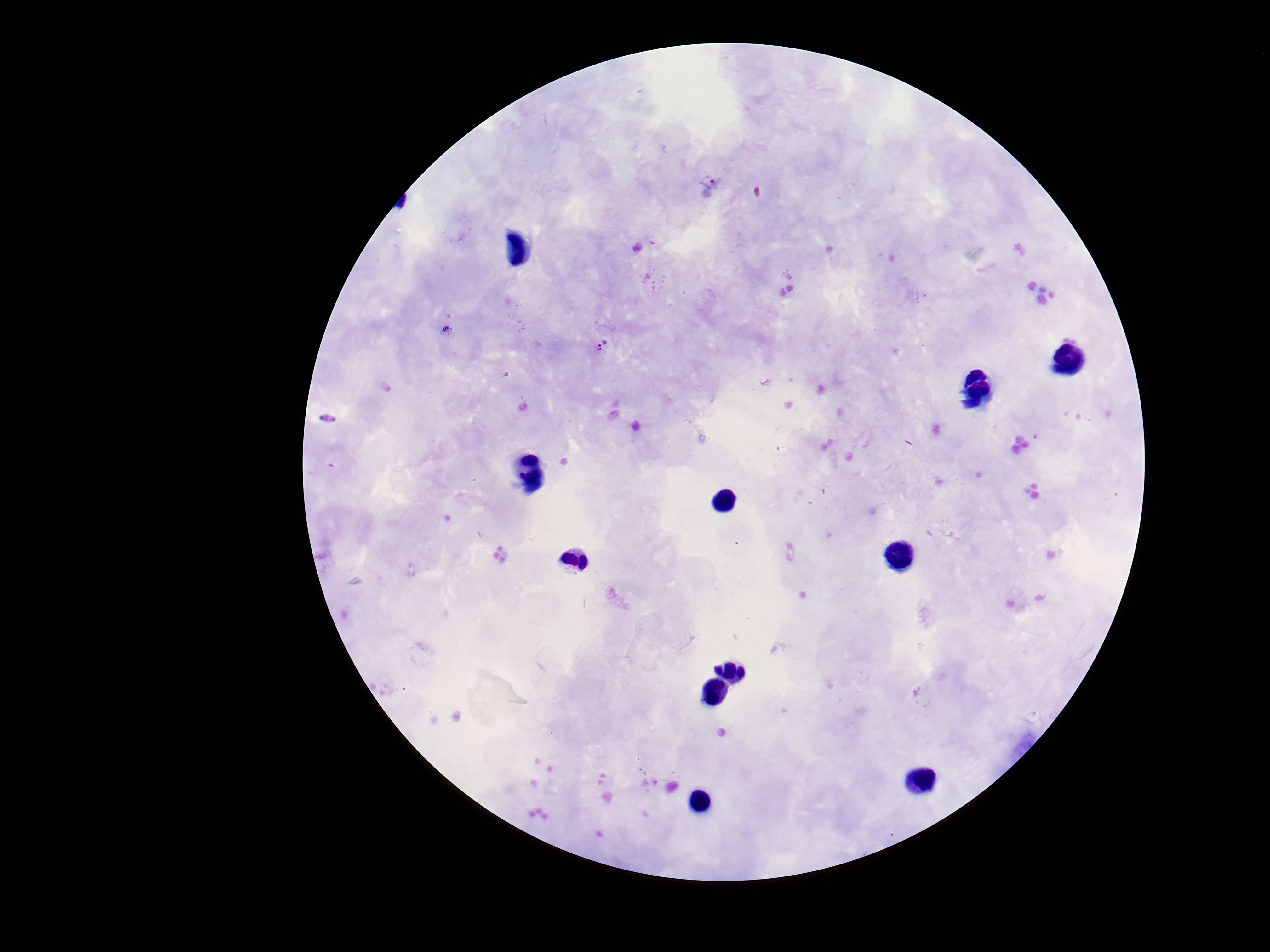
Approximate centers as {x, y} in pixels. Plasmodium parasite locations: {708, 180}, {599, 347}. Photographed through the microscope eyepiece with a smartphone camera. Image is 1270×952 pixels. Patient malaria status: positive. Thick blood smear. One field from this slide. 100x magnification. Giemsa-stained preparation.